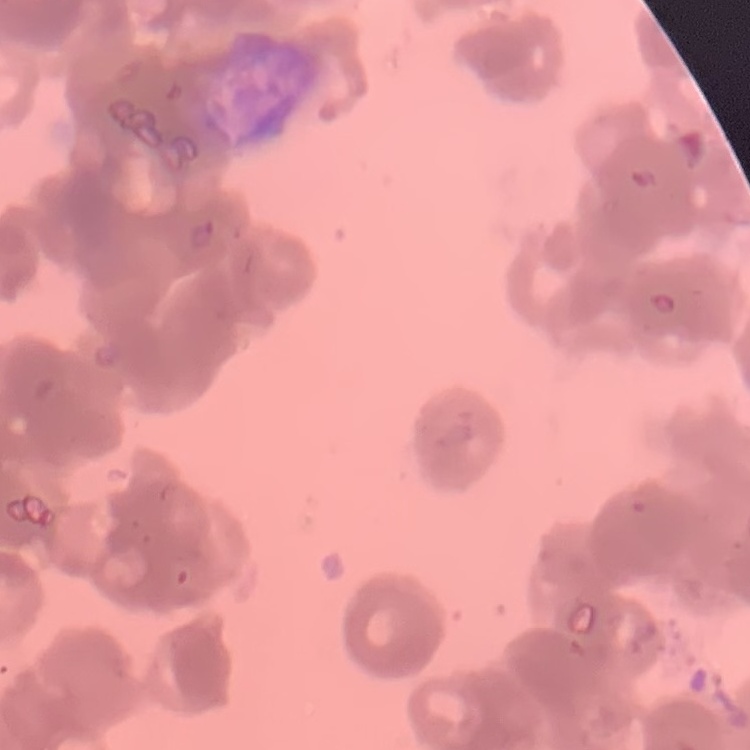

red blood cell morphology = rouleaux formation
image type = one tile cut from a larger photomicrograph
stain = Field's or Giemsa
preparation = thin peripheral smear